Name the parasite shown.
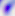

Toxoplasma gondii.

Captured at 400x magnification. Micrograph.